Report the malaria status of this cell.
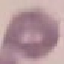

Uninfected.

Summary:
  - Image type: automatically extracted cell patch, resized to 64 × 64 pixels
  - Stain: Giemsa
  - Capture: smartphone camera at the microscope eyepiece
  - Preparation: thin blood smear